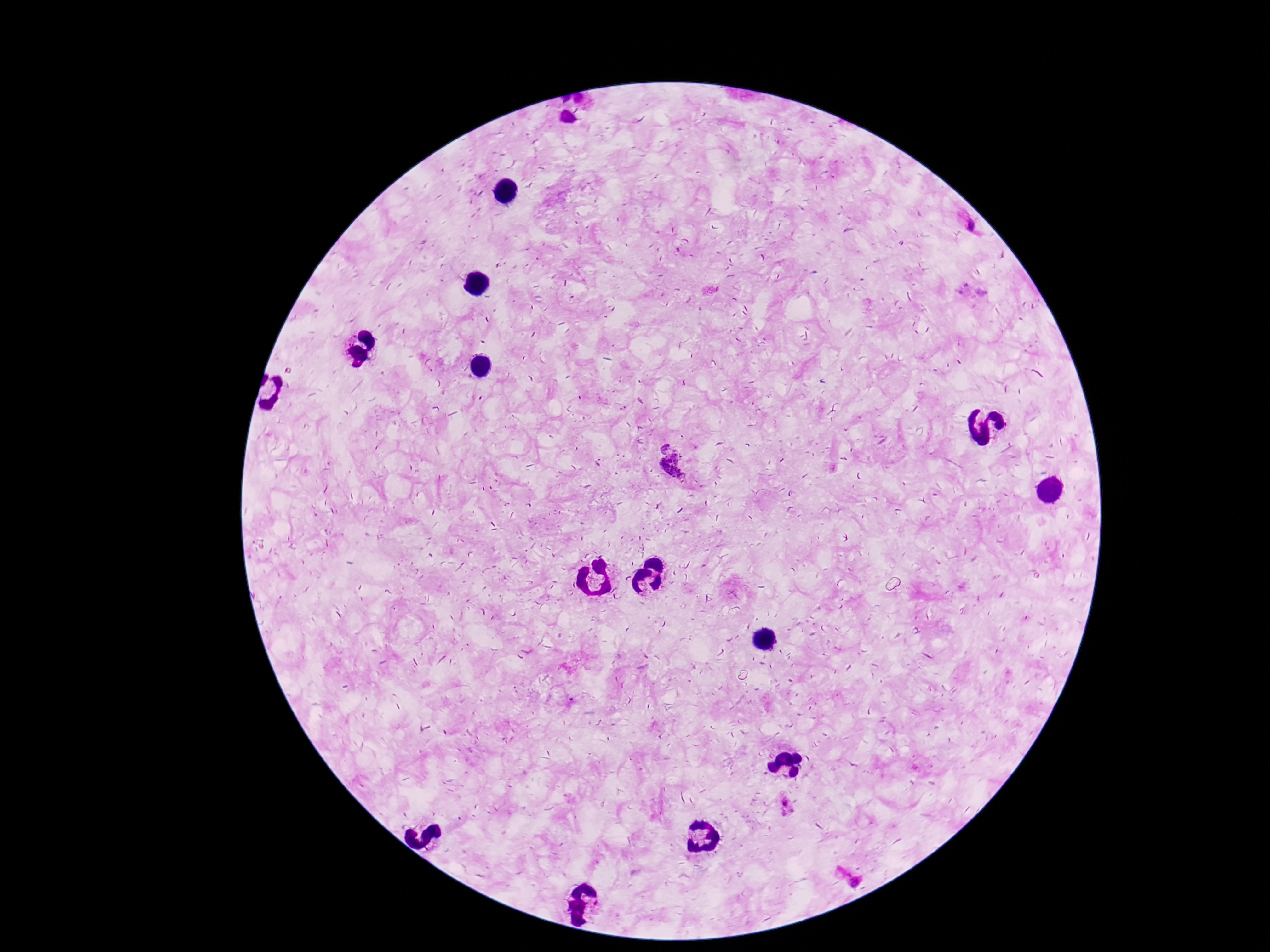 Approximate object centers, in pixels from the top-left corner. Plasmodium parasite locations: (x=971, y=226), (x=970, y=293), (x=661, y=445), (x=674, y=468), (x=786, y=806), (x=843, y=874), (x=855, y=882). 100x magnification. Giemsa-stained preparation. Single field of view. Photographed through the microscope eyepiece with a smartphone camera. Patient malaria status: positive. Thick blood film. Image is 1270×952 pixels.